Locate every leukocyte (white blood cell).
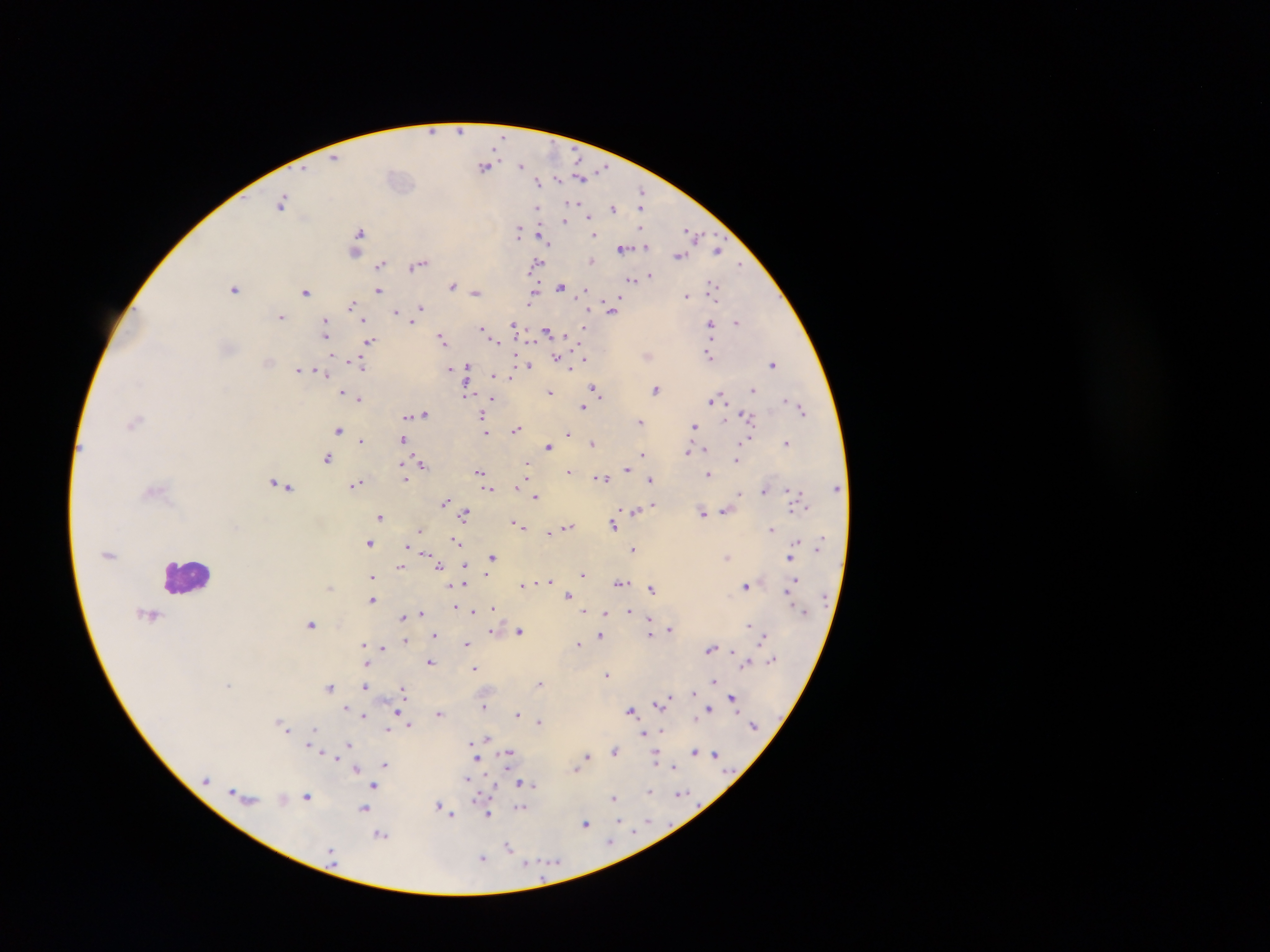
Approximate centers as x y in pixels.
Leukocytes: 186 575.

Malaria parasite locations: 460 131; 432 132; 335 157; 485 166; 522 166; 581 176; 538 182; 642 192; 282 202; 572 202; 641 205; 612 208; 537 209; 589 218; 564 220; 518 230; 642 230; 359 232; 692 232; 595 234; 544 238; 645 246; 623 249; 719 250; 355 251; 679 256; 591 260; 536 263; 381 264; 417 265; 740 266; 649 275; 633 280; 452 285; 561 286; 712 286; 234 288; 379 290; 306 291; 585 291; 476 293; 533 294; 686 296; 351 305; 421 307; 612 309; 396 312; 281 316; 414 318; 363 320; 410 320; 738 321; 325 323; 710 324; 514 326; 482 327; 584 328; 326 330; 547 331; 442 340; 497 341; 371 342; 367 346; 708 356; 556 358; 585 359; 564 362; 360 364; 773 364; 530 365; 467 367; 450 369; 299 370; 325 374; 494 375; 511 376; 595 389; 656 389; 753 390; 549 391; 343 392; 465 393; 359 399; 492 399; 785 399; 711 400; 582 408; 802 410; 424 414; 408 416; 482 416; 748 416; 725 420; 135 421; 641 421; 693 425; 484 427; 516 429; 338 430; 486 431; 569 434; 403 440; 747 440; 361 441; 787 442; 593 443; 549 446; 703 450; 688 452; 642 454; 327 458; 736 460; 422 464; 525 465; 402 467; 627 469; 570 471; 480 473; 709 474; 601 478; 406 479; 651 479; 357 484; 281 485; 516 486; 488 489; 789 489; 763 490; 740 494; 536 496; 444 502; 652 504; 636 510; 725 511; 702 512; 465 514; 380 517; 516 523; 613 525; 521 526; 567 526; 772 530; 420 531; 554 531; 549 533; 459 542; 369 543; 408 545; 634 549; 414 551; 426 553; 492 557; 727 557; 790 559; 439 566; 466 566; 400 567; 488 573; 583 575; 372 576; 549 581; 464 583; 621 583; 523 585; 745 585; 330 588; 652 589; 791 589; 568 595; 372 599; 454 606; 494 608; 629 610; 584 612; 605 612; 422 613; 474 613; 402 616; 311 623; 748 625; 669 629; 491 631; 520 631; 649 633; 434 634; 600 635; 764 635; 406 640; 467 643; 363 644; 578 644; 383 647; 712 648; 772 659; 430 662; 746 663; 475 668; 606 674; 713 680; 539 683; 229 684; 365 686; 329 687; 403 689; 693 692; 669 696; 732 697; 665 698; 660 702; 485 706; 346 708; 709 709; 631 710; 397 711; 440 713; 518 714; 363 716; 539 721; 409 725; 284 726; 313 730; 388 730; 644 733; 487 738; 348 743; 471 743; 311 745; 615 750; 695 751; 510 752; 714 754; 587 756; 655 759; 478 760; 385 763; 673 767; 576 768; 356 769; 467 780; 521 784; 374 785; 649 791; 233 792; 680 795; 307 797; 614 798; 283 799; 440 806; 364 808; 520 808; 488 813; 450 814; 617 821; 585 823; 380 834; 611 842; 509 846; 482 858. Image is 1270×952 pixels. Collected in Ghana. One field of view. Photographed through a microscope with a mobile-phone camera. Thick blood smear.